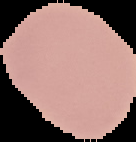
preparation: thin blood smear
result: no Plasmodium parasites seen
image_size: 136×142 pixels
image_type: cell region segmented out of the field of view; surrounding area masked to black